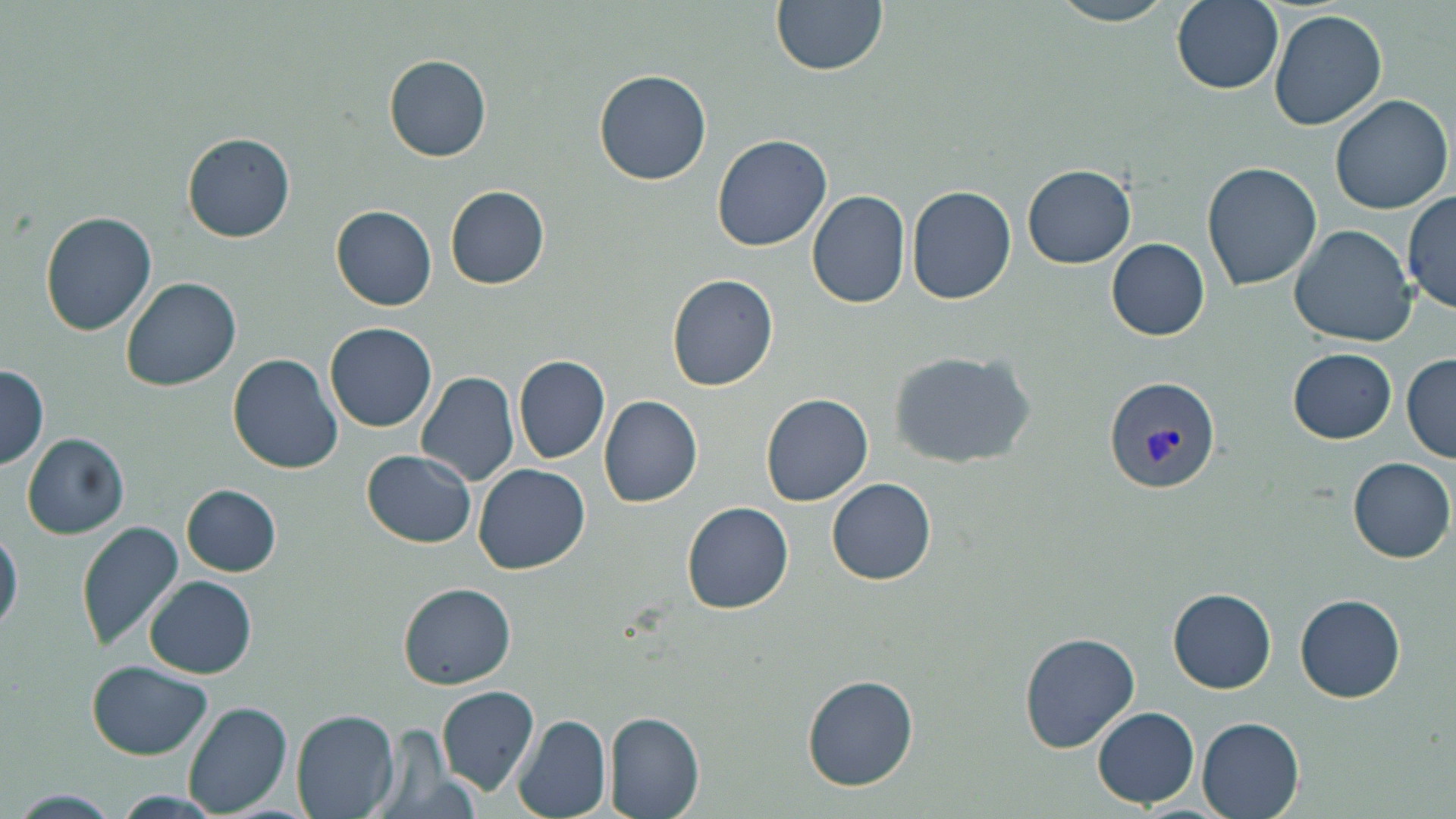

{
  "slide_level_diagnosis": "Plasmodium vivax",
  "magnification": "1000x",
  "plasmodium_vivax_infected_red_blood_cell_locations": "approximate bounding boxes as named x1/y1/x2/y2 corners in pixels: (x1=1103, y1=374, x2=1221, y2=494)",
  "stain": "May-Grünwald-Giemsa",
  "preparation": "thin blood smear",
  "uninfected_red_blood_cell_locations": "approximate bounding boxes as named x1/y1/x2/y2 corners in pixels: (x1=770, y1=0, x2=888, y2=78), (x1=1044, y1=0, x2=1178, y2=25), (x1=1172, y1=0, x2=1283, y2=95), (x1=1268, y1=9, x2=1389, y2=132), (x1=383, y1=54, x2=492, y2=162), (x1=592, y1=70, x2=712, y2=186), (x1=1329, y1=94, x2=1453, y2=215), (x1=181, y1=133, x2=296, y2=244), (x1=713, y1=135, x2=833, y2=253), (x1=1201, y1=162, x2=1322, y2=292), (x1=1022, y1=164, x2=1136, y2=270), (x1=444, y1=185, x2=549, y2=290), (x1=905, y1=185, x2=1017, y2=304), (x1=806, y1=191, x2=910, y2=309), (x1=1402, y1=193, x2=1456, y2=314), (x1=330, y1=205, x2=437, y2=311), (x1=39, y1=212, x2=157, y2=336), (x1=1287, y1=225, x2=1416, y2=348), (x1=1105, y1=239, x2=1210, y2=340), (x1=666, y1=273, x2=779, y2=392), (x1=121, y1=275, x2=242, y2=393), (x1=324, y1=321, x2=438, y2=432), (x1=1288, y1=348, x2=1395, y2=444), (x1=887, y1=350, x2=1035, y2=470), (x1=227, y1=354, x2=343, y2=475), (x1=1401, y1=354, x2=1456, y2=463), (x1=513, y1=355, x2=610, y2=464), (x1=1, y1=365, x2=48, y2=468), (x1=415, y1=373, x2=518, y2=488), (x1=761, y1=392, x2=873, y2=506), (x1=599, y1=396, x2=703, y2=508), (x1=22, y1=432, x2=129, y2=539), (x1=363, y1=450, x2=476, y2=549), (x1=1348, y1=457, x2=1454, y2=563), (x1=473, y1=463, x2=591, y2=575), (x1=826, y1=479, x2=937, y2=586), (x1=181, y1=485, x2=282, y2=576), (x1=682, y1=502, x2=794, y2=615), (x1=77, y1=522, x2=184, y2=652), (x1=0, y1=529, x2=23, y2=634), (x1=144, y1=575, x2=257, y2=679), (x1=398, y1=582, x2=518, y2=690), (x1=1167, y1=588, x2=1277, y2=694), (x1=1295, y1=593, x2=1404, y2=703), (x1=1018, y1=631, x2=1141, y2=754), (x1=87, y1=660, x2=213, y2=760), (x1=800, y1=675, x2=920, y2=792), (x1=436, y1=686, x2=538, y2=795), (x1=183, y1=701, x2=293, y2=816), (x1=1093, y1=706, x2=1199, y2=809), (x1=291, y1=711, x2=400, y2=819), (x1=605, y1=712, x2=705, y2=819), (x1=511, y1=714, x2=610, y2=819), (x1=1197, y1=717, x2=1304, y2=819), (x1=13, y1=790, x2=122, y2=818), (x1=107, y1=791, x2=228, y2=818)",
  "modality": "light microscopy",
  "field_of_view": "one of a larger specimen",
  "image_size": "1456×819 pixels"
}